Describe the morphology of the red blood cells.
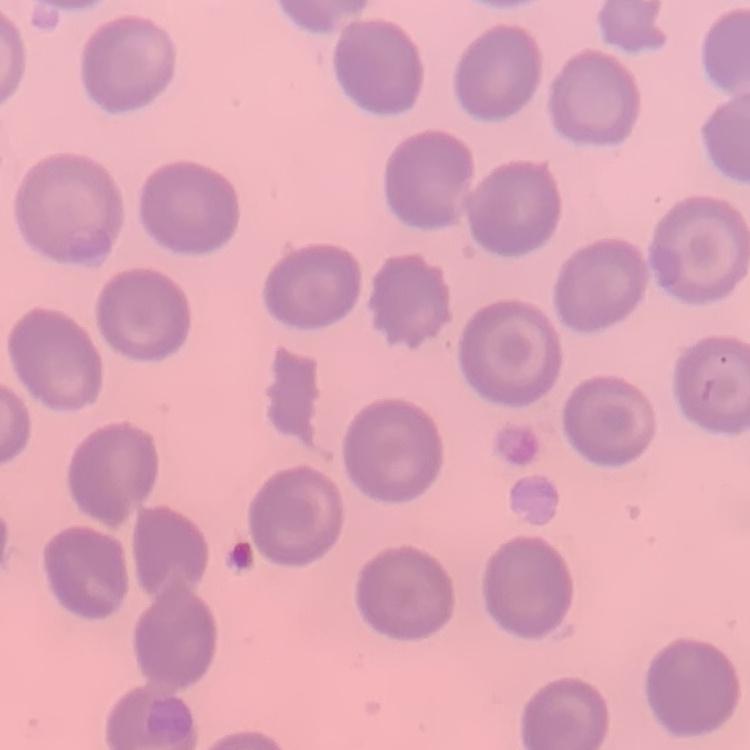
No rouleaux formation.

Summary:
  - Preparation: thin blood smear
  - Image type: one tile cut from a larger photomicrograph
  - Stain: Field's or Giemsa